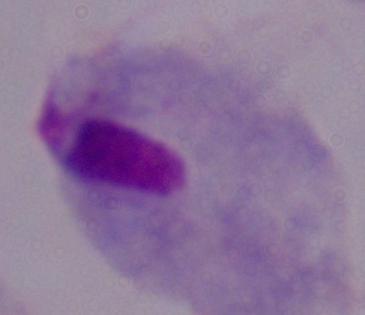

Summary:
  - Modality: micrograph
  - Identification: trichomonad
  - Magnification: 1000x